Name the parasite shown.
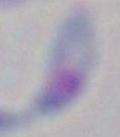
This is Toxoplasma gondii.

Summary:
  - Magnification: 1000x
  - Modality: photomicrograph